Report the malaria status of this cell.
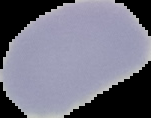
Uninfected.

preparation = thin blood smear
image size = 151×118 pixels
image type = segmented cell region on a black background